Classify this cell by malaria status.
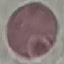

It is uninfected.

stain = Giemsa
preparation = thin blood film
image type = automatically extracted cell patch, resized to 64 × 64 pixels
capture = smartphone through the microscope eyepiece